Classify this cell by malaria status.
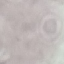
It is uninfected.

stain: Giemsa
image_type: automatically extracted cell patch, resized to 64 × 64 pixels
preparation: thin smear
capture: smartphone camera at the microscope eyepiece